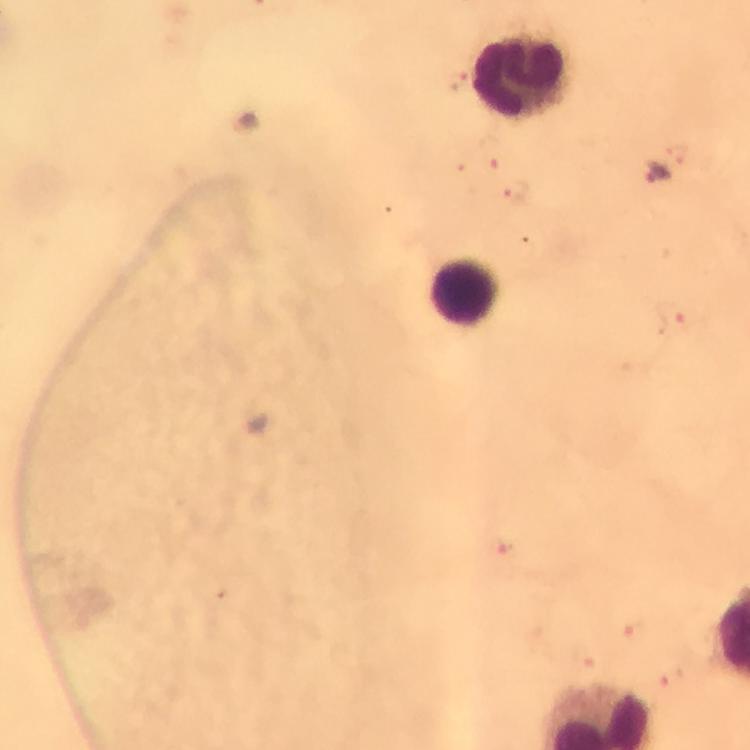
leukocyte_locations: 'approximate centers as {x, y} in pixels: {522, 78}, {465, 295}'
immersion_oil: applied
context: from a malaria diagnostic workup
stain: Giemsa
malaria_parasite_locations: 'approximate centers as {x, y} in pixels: {654, 175}'
magnification: 100x
image_size: 750×750 pixels
capture: smartphone mounted on the microscope
preparation: thick smear
cropped_from: one field of view